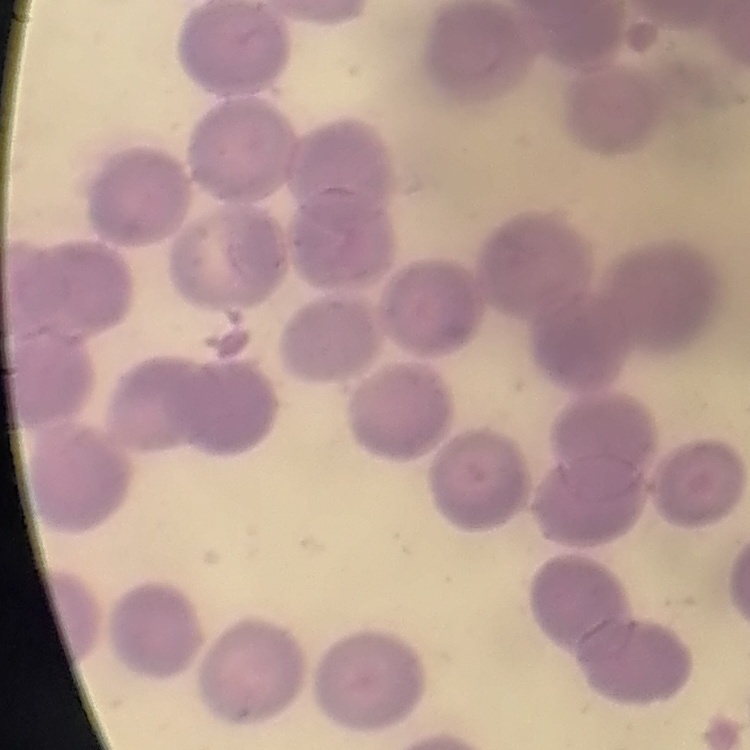
The red blood cells exhibit no rouleaux formation. Square crop of a larger photomicrograph. Stained with either Field's or Giemsa. Thin blood smear.